Locate and identify every blood parasite.
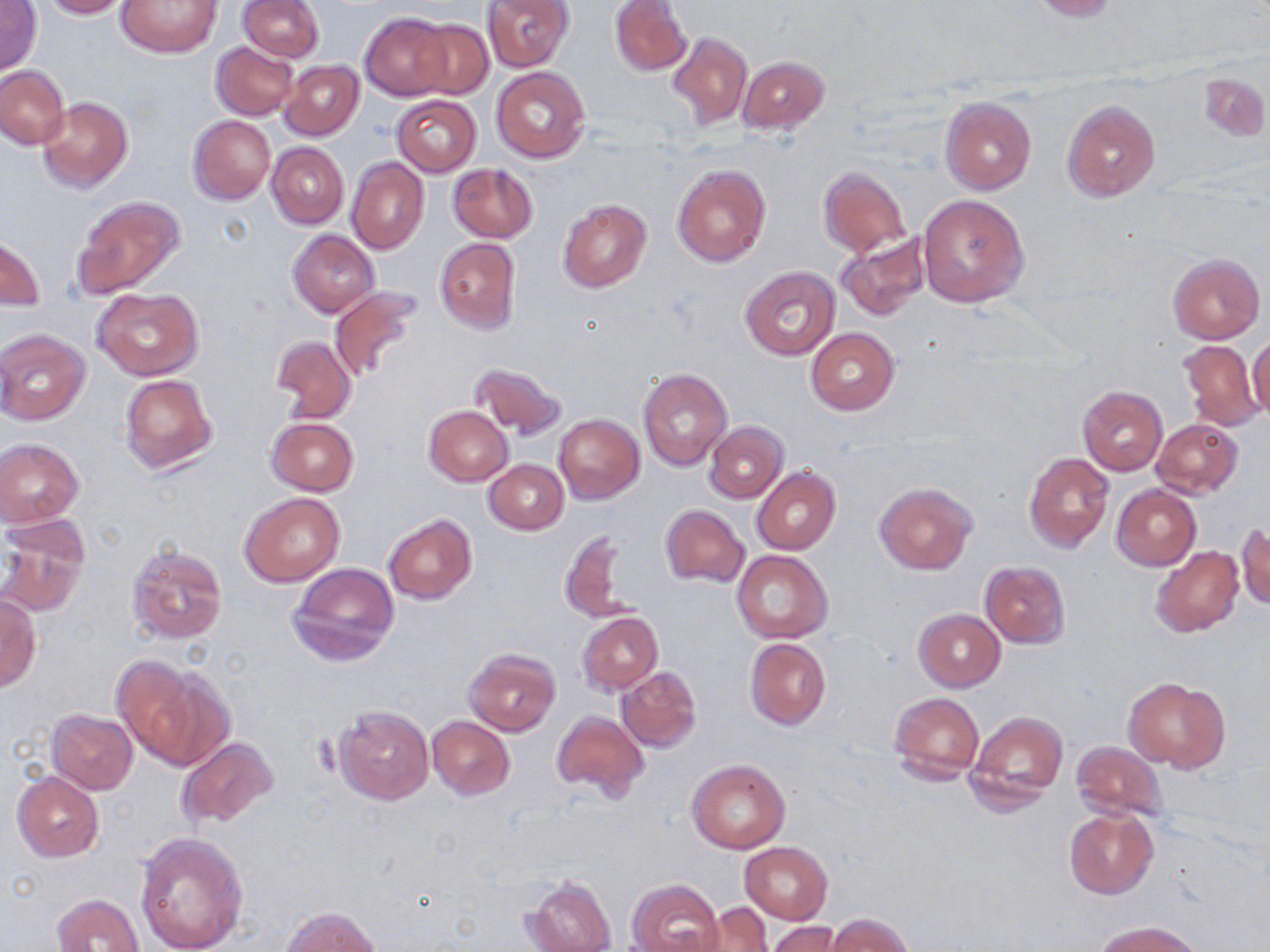
No blood parasites observed.

slide-level diagnosis = no evidence of blood parasites
modality = optical microscopy
magnification = 1000x
image size = 1270×952 pixels
stain = May-Grünwald-Giemsa
uninfected red blood cell locations = approximate bounding boxes as (x1,y1)-(x2,y2) corner pairs in pixels: (0,0)-(41,77), (37,0)-(134,18), (116,0)-(222,57), (238,0)-(324,62), (482,0)-(573,70), (610,0)-(691,76), (1022,0)-(1121,21), (361,12)-(455,100), (409,19)-(492,100), (667,32)-(752,129), (211,42)-(299,120), (738,57)-(829,133), (279,60)-(363,141), (0,66)-(69,149), (491,67)-(589,163), (1197,69)-(1269,142), (391,94)-(482,176), (38,96)-(133,193), (940,97)-(1036,194), (1061,99)-(1161,203), (188,115)-(275,205), (267,142)-(348,228), (347,157)-(429,255), (672,162)-(772,268), (448,163)-(538,243), (818,166)-(910,256), (917,194)-(1029,306), (73,195)-(185,298), (559,199)-(652,293), (288,229)-(381,317), (836,232)-(930,322), (1,234)-(44,308), (433,238)-(522,335), (1167,253)-(1265,343), (739,266)-(840,360), (329,285)-(425,383), (92,289)-(203,381), (0,328)-(90,424), (806,328)-(898,414), (1248,334)-(1270,418), (270,337)-(356,424), (1177,339)-(1264,431), (468,361)-(567,441), (638,368)-(733,471), (437,372)-(558,476), (119,373)-(218,475), (1076,386)-(1168,476), (424,406)-(512,486), (553,413)-(645,503), (266,417)-(358,496), (1151,417)-(1243,498), (704,422)-(788,503), (0,438)-(83,528), (1024,452)-(1113,553), (486,460)-(568,534), (752,467)-(839,555), (873,482)-(977,574), (1111,485)-(1200,570), (239,493)-(346,587), (659,504)-(748,587), (383,514)-(477,604), (1236,521)-(1269,610), (0,528)-(88,616), (559,529)-(634,623), (126,543)-(226,644), (1150,546)-(1244,638), (732,550)-(833,643), (980,561)-(1070,647), (288,562)-(399,667), (0,596)-(41,691), (913,609)-(1004,691), (577,612)-(662,695), (745,638)-(832,730), (464,647)-(560,737), (111,655)-(220,767), (616,665)-(701,753), (1124,677)-(1230,772), (889,692)-(984,785), (334,705)-(433,805), (47,710)-(137,794), (551,711)-(649,803), (968,711)-(1069,806), (428,717)-(515,799), (176,737)-(280,830), (1071,741)-(1168,822), (686,759)-(790,853), (11,771)-(104,862), (1064,809)-(1158,899), (135,834)-(248,952), (740,841)-(833,923), (524,875)-(616,952), (627,878)-(723,952), (52,893)-(144,952), (699,902)-(773,951), (281,906)-(381,951), (827,914)-(913,952), (1093,920)-(1202,952), (769,921)-(841,952)
preparation = thin blood smear
field of view = single